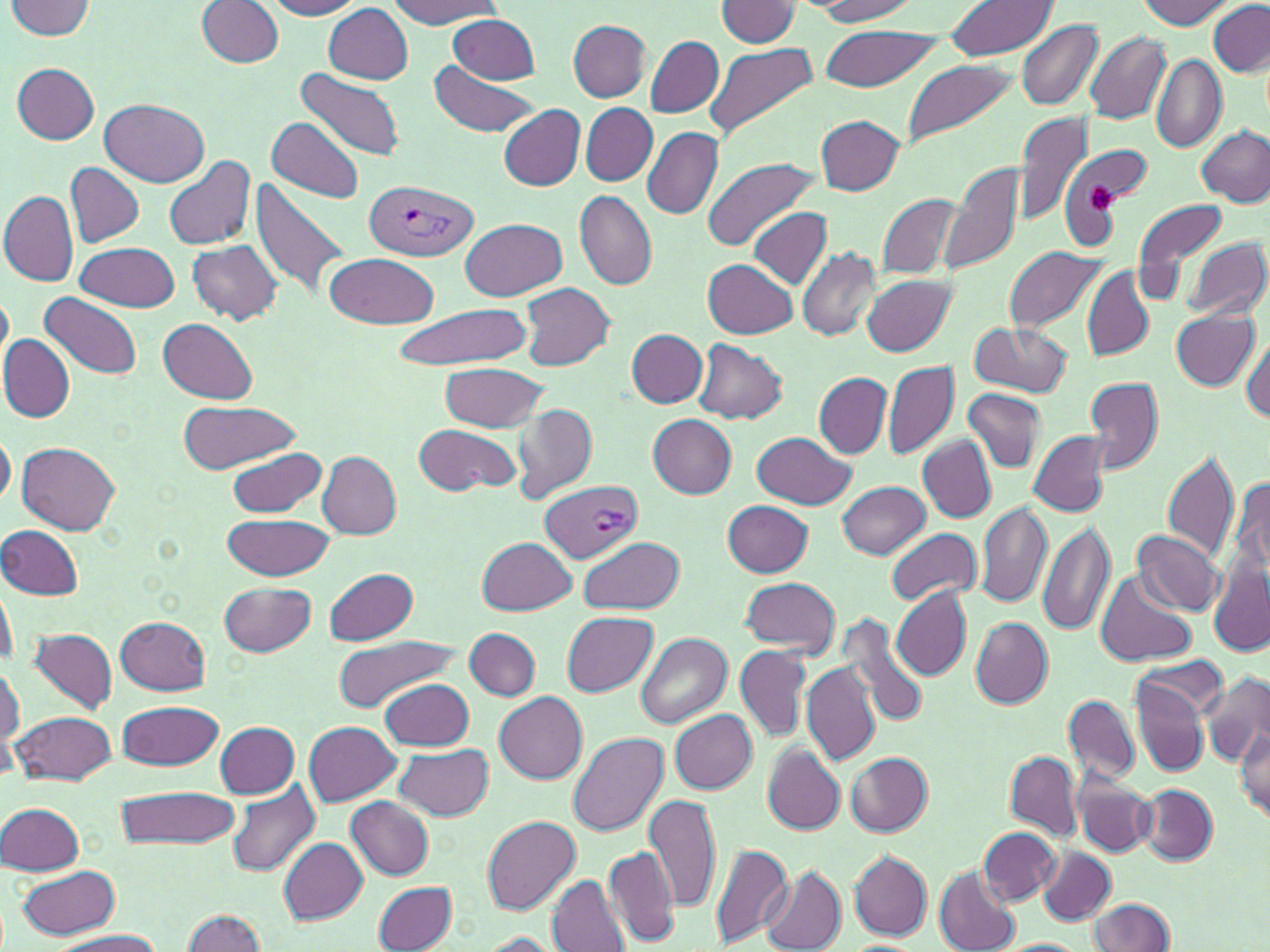
Summary:
  - Coordinate format: approximate bounding boxes as (x1,y1)-(x2,y2) corner pairs in pixels
  - Uninfected red blood cell locations: (6,0)-(96,40), (264,0)-(365,19), (814,0)-(920,23), (1137,0)-(1235,28), (197,1)-(284,68), (382,1)-(502,27), (713,1)-(800,47), (946,1)-(1057,62), (1207,2)-(1270,76), (325,5)-(413,83), (449,14)-(540,84), (1017,19)-(1102,112), (568,21)-(651,100), (819,25)-(941,91), (1086,32)-(1170,124), (647,35)-(723,119), (704,41)-(816,141), (1151,53)-(1226,153), (899,58)-(1018,151), (429,61)-(537,137), (12,63)-(100,144), (296,67)-(405,163), (99,99)-(209,186), (500,104)-(585,191), (582,104)-(657,185), (1012,109)-(1093,228), (816,116)-(905,195), (267,118)-(365,203), (1197,125)-(1270,207), (643,126)-(723,220), (164,153)-(256,250), (701,155)-(819,252), (943,160)-(1028,278), (65,164)-(144,248), (248,174)-(356,304), (0,191)-(77,287), (878,191)-(968,282), (573,192)-(657,291), (1134,200)-(1227,284), (748,207)-(831,288), (460,218)-(567,301), (1186,237)-(1269,322), (187,239)-(284,326), (76,241)-(180,313), (1003,246)-(1109,336), (797,247)-(883,342), (326,254)-(439,329), (703,257)-(798,338), (1083,267)-(1152,360), (863,275)-(955,357), (519,281)-(615,372), (0,287)-(12,376), (41,293)-(141,380), (390,303)-(532,371), (1170,308)-(1259,391), (158,318)-(257,404), (969,322)-(1072,399), (627,330)-(708,407), (1241,335)-(1270,424), (0,336)-(73,422), (693,339)-(787,423), (883,360)-(959,461), (441,362)-(547,433), (814,372)-(892,459), (1085,375)-(1164,475), (964,389)-(1044,471), (176,403)-(300,470), (510,403)-(596,501), (647,414)-(737,498), (415,422)-(522,495), (0,427)-(15,508), (1028,430)-(1112,516), (751,431)-(855,509), (918,437)-(996,522), (18,441)-(123,533), (226,447)-(328,519), (1161,448)-(1239,564), (318,452)-(401,539), (1228,472)-(1270,595), (838,480)-(929,559), (722,500)-(813,577), (975,501)-(1052,610), (223,512)-(336,580), (1036,519)-(1114,637), (1,525)-(84,599), (885,528)-(982,606), (1132,530)-(1223,617), (478,537)-(575,616), (580,537)-(684,615), (1208,560)-(1269,657), (325,569)-(419,645), (1095,569)-(1196,667), (1,570)-(16,672), (740,576)-(839,657), (219,581)-(317,657), (891,586)-(970,680), (563,613)-(658,697), (116,616)-(210,695), (839,617)-(930,729), (970,617)-(1052,708), (466,628)-(540,699), (26,629)-(118,716), (637,633)-(732,728), (331,636)-(459,714), (734,643)-(812,741), (1137,651)-(1229,719), (802,660)-(881,765), (1,662)-(22,751), (1200,673)-(1270,766), (1130,675)-(1211,778), (379,678)-(475,752), (494,692)-(588,783), (1064,695)-(1139,784), (118,700)-(222,769), (11,709)-(117,786), (669,709)-(758,792), (216,722)-(300,797), (303,722)-(401,805), (1235,723)-(1269,819), (568,733)-(668,836), (395,743)-(494,821), (763,745)-(845,835), (1007,752)-(1082,842), (847,754)-(933,836), (1072,768)-(1156,858), (227,782)-(322,877), (1139,785)-(1217,865), (115,786)-(238,850), (646,792)-(720,915), (345,796)-(433,879), (0,802)-(84,877), (244,803)-(360,914), (483,816)-(580,914), (978,827)-(1061,905), (278,836)-(368,926), (708,842)-(792,948), (1038,846)-(1114,926), (605,847)-(682,945), (849,850)-(932,941), (15,865)-(122,940), (761,867)-(846,952), (934,869)-(1019,951), (546,874)-(629,952), (375,881)-(457,951), (1088,897)-(1176,951), (181,910)-(269,952), (49,929)-(168,952), (477,932)-(562,952), (993,939)-(1092,951)
  - Plasmodium vivax-infected red blood cell locations: (364,179)-(479,261), (540,482)-(642,562)
  - Platelet locations: (1086,186)-(1118,218)
  - Slide-level diagnosis: Plasmodium vivax
  - Stain: May-Grünwald-Giemsa
  - Field of view: one of a larger specimen
  - Preparation: thin blood film
  - Image size: 1270×952 pixels
  - Magnification: 1000x
  - Modality: light microscopy